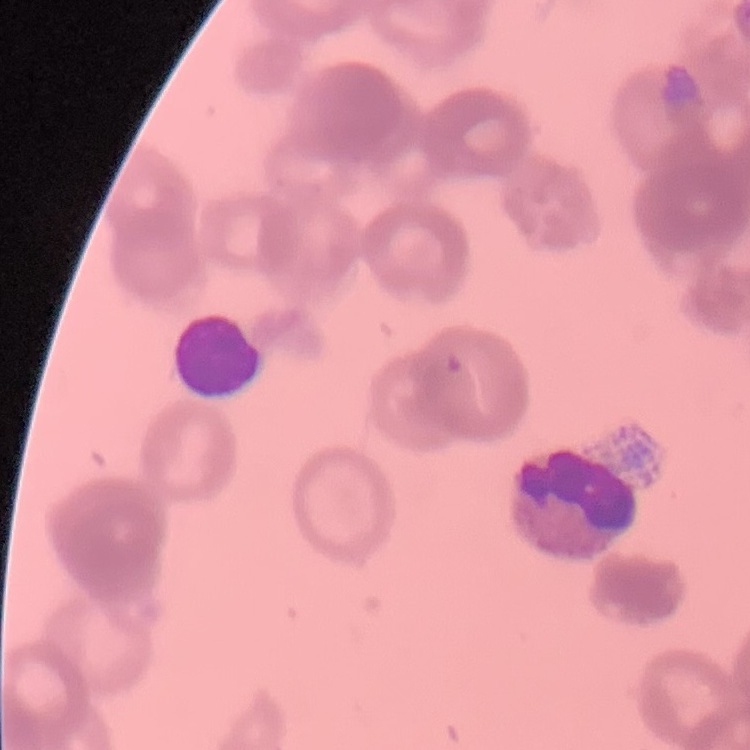

Summary:
  - Erythrocyte morphology: rouleaux formation
  - Image type: one tile cut from a larger photomicrograph
  - Preparation: thin blood film
  - Stain: Field's or Giemsa